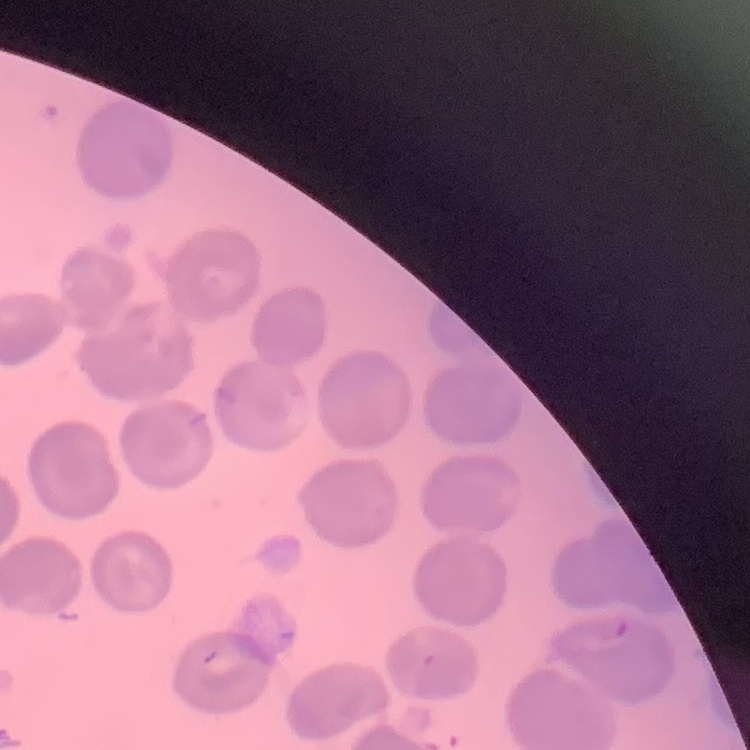
Summary:
  - Erythrocyte morphology: no rouleaux formation
  - Image type: square crop of a larger photomicrograph
  - Preparation: thin blood smear
  - Stain: Field's or Giemsa